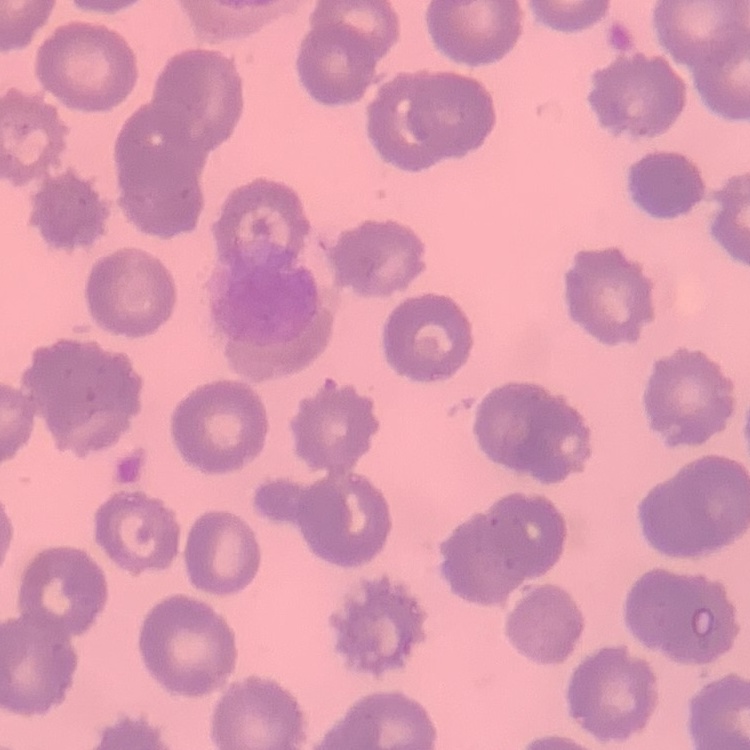

Summary:
  - Erythrocyte morphology: no rouleaux formation
  - Preparation: thin peripheral smear
  - Stain: Field's or Giemsa
  - Image type: one tile cut from a larger photomicrograph